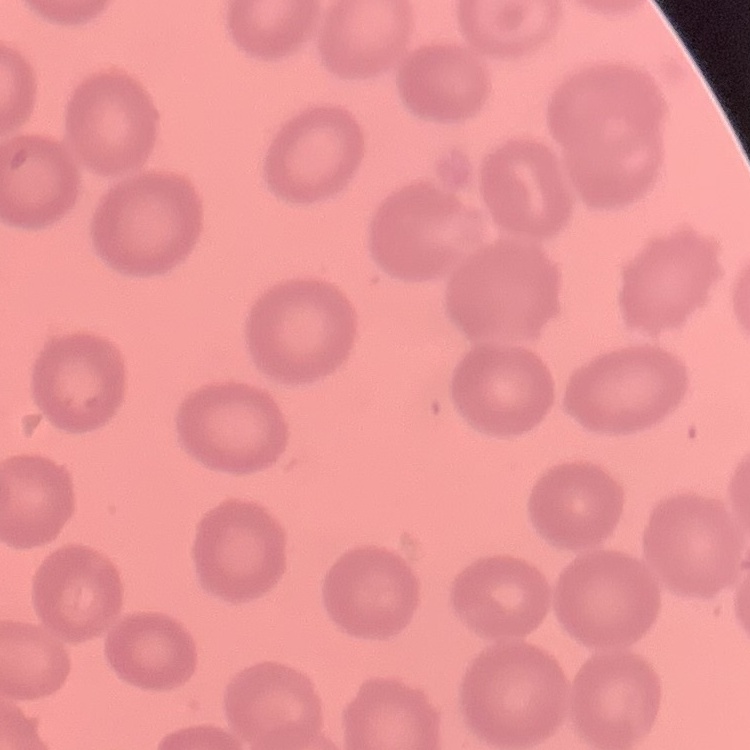 The erythrocytes exhibit no rouleaux formation. Thin blood film. Field's or Giemsa stain. Square crop of a larger photomicrograph.